Outline each Plasmodium ovale-infected red blood cell.
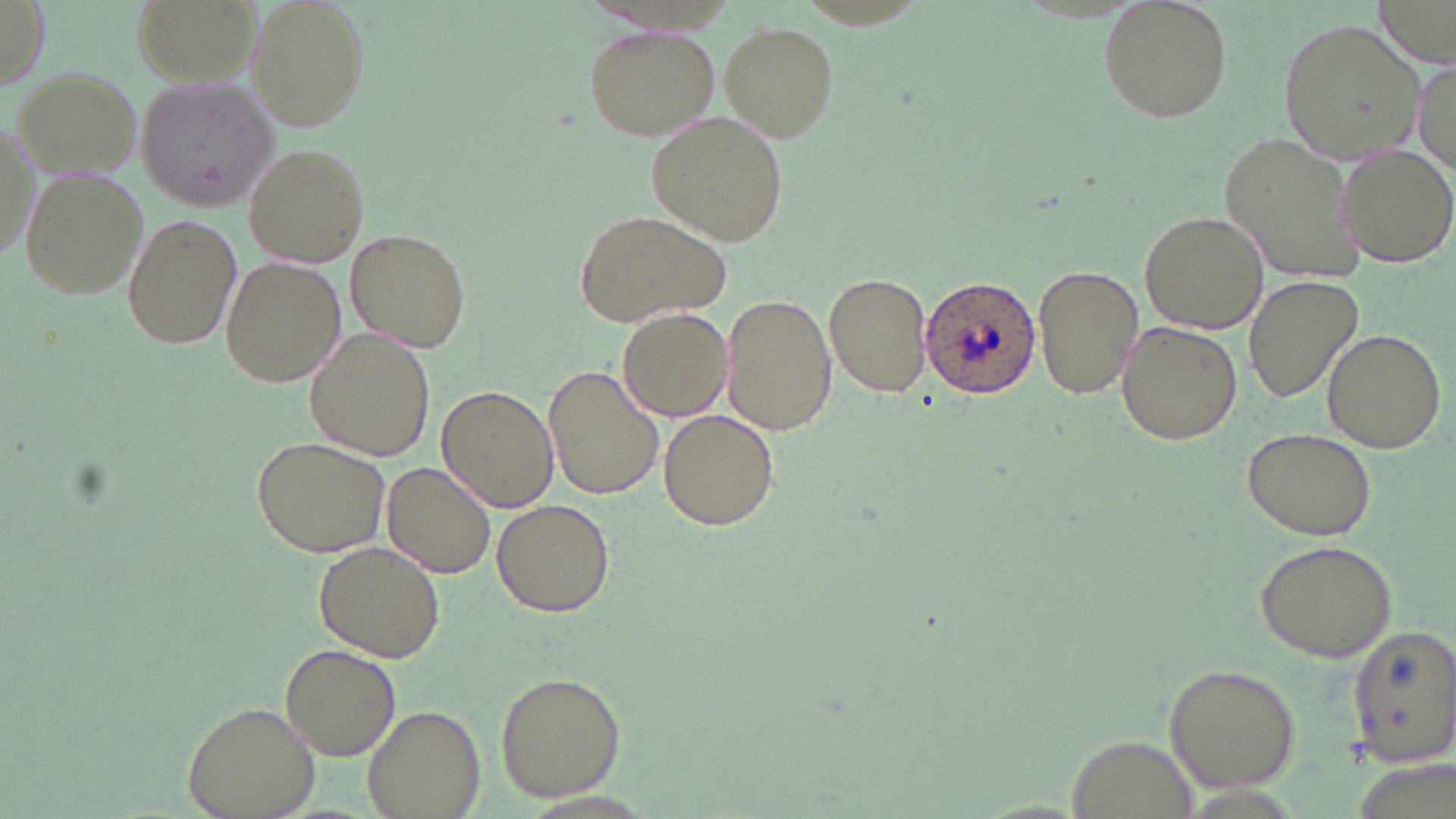

Approximate bounding boxes as named x1/y1/x2/y2 corners in pixels.
Plasmodium ovale-infected red blood cells: (x1=917, y1=274, x2=1041, y2=402).

slide_level_diagnosis: Plasmodium ovale
magnification: 1000x
stain: May-Grünwald-Giemsa
image_size: 1456×819 pixels
uninfected_red_blood_cell_locations: 'approximate bounding boxes as named x1/y1/x2/y2 corners in pixels: (x1=0, y1=0, x2=49, y2=88), (x1=247, y1=0, x2=369, y2=132), (x1=1098, y1=1, x2=1233, y2=122), (x1=1373, y1=1, x2=1452, y2=66), (x1=1279, y1=17, x2=1430, y2=166), (x1=721, y1=22, x2=836, y2=140), (x1=583, y1=25, x2=720, y2=139), (x1=1412, y1=62, x2=1455, y2=184), (x1=11, y1=65, x2=144, y2=180), (x1=135, y1=76, x2=281, y2=211), (x1=648, y1=110, x2=786, y2=248), (x1=1, y1=112, x2=42, y2=272), (x1=1218, y1=131, x2=1367, y2=283), (x1=1333, y1=141, x2=1456, y2=266), (x1=244, y1=142, x2=371, y2=266), (x1=21, y1=167, x2=148, y2=301), (x1=572, y1=208, x2=733, y2=328), (x1=1140, y1=210, x2=1269, y2=333), (x1=122, y1=212, x2=242, y2=351), (x1=345, y1=228, x2=471, y2=354), (x1=221, y1=256, x2=342, y2=390), (x1=1031, y1=264, x2=1143, y2=400), (x1=823, y1=272, x2=933, y2=397), (x1=1242, y1=273, x2=1364, y2=403), (x1=722, y1=292, x2=833, y2=436), (x1=616, y1=307, x2=734, y2=421), (x1=1115, y1=322, x2=1242, y2=445), (x1=1320, y1=327, x2=1448, y2=452), (x1=306, y1=328, x2=437, y2=461), (x1=547, y1=364, x2=669, y2=501), (x1=436, y1=384, x2=559, y2=513), (x1=659, y1=409, x2=779, y2=532), (x1=1238, y1=426, x2=1379, y2=542), (x1=251, y1=435, x2=389, y2=556), (x1=381, y1=463, x2=496, y2=579), (x1=491, y1=498, x2=616, y2=617), (x1=1250, y1=538, x2=1398, y2=662), (x1=312, y1=543, x2=444, y2=660), (x1=1346, y1=626, x2=1456, y2=768), (x1=278, y1=646, x2=401, y2=762), (x1=1163, y1=662, x2=1301, y2=791), (x1=494, y1=671, x2=625, y2=802), (x1=184, y1=700, x2=319, y2=819), (x1=363, y1=704, x2=486, y2=818), (x1=1066, y1=732, x2=1201, y2=818)'
preparation: thin blood smear
field_of_view: single
modality: light microscopy